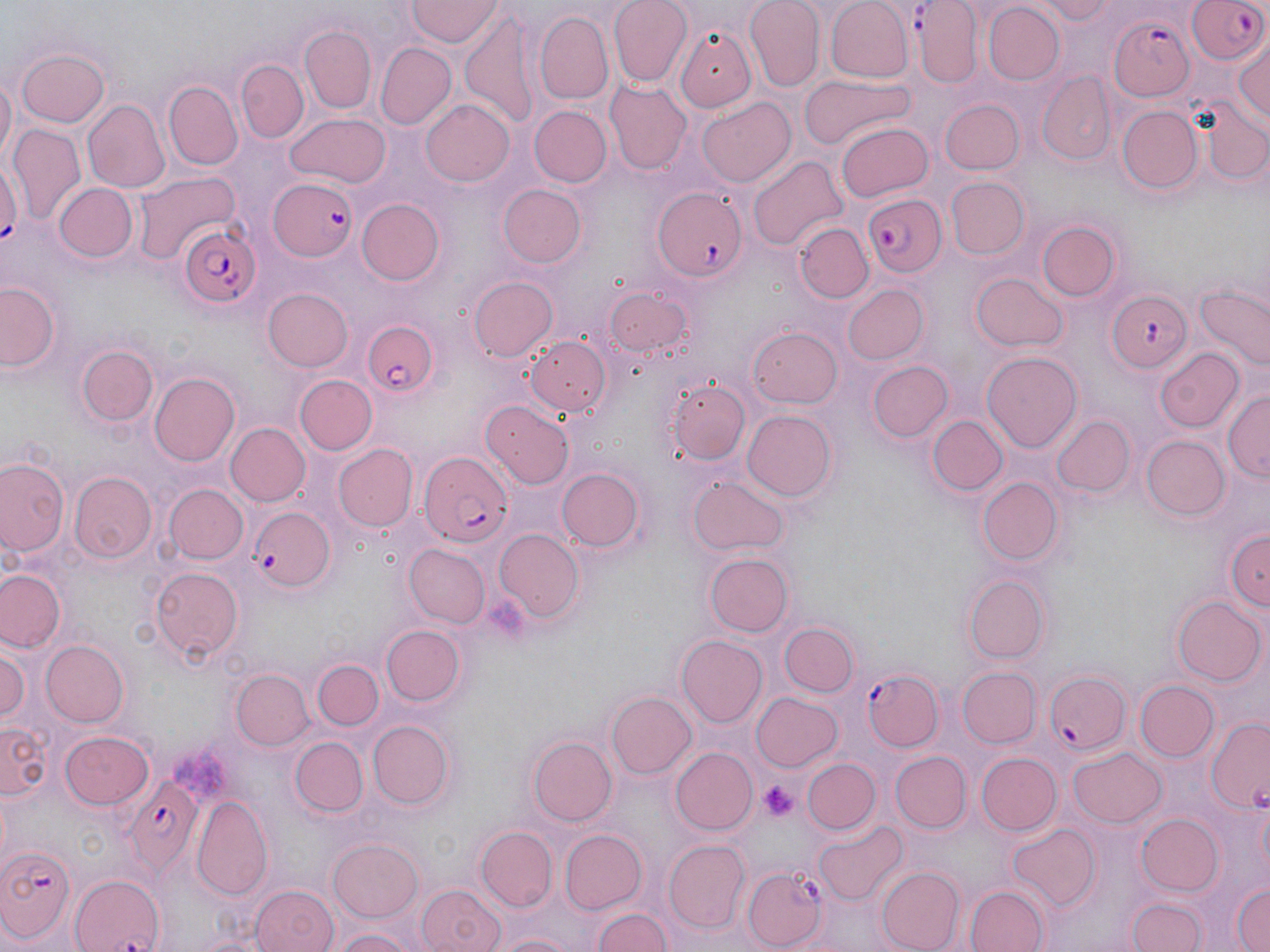
Summary:
  - Coordinate format: approximate bounding boxes as named x1/y1/x2/y2 corners in pixels
  - Platelet locations: (x1=759, y1=781, x2=801, y2=821)
  - Uninfected red blood cell locations: (x1=609, y1=0, x2=690, y2=85), (x1=746, y1=0, x2=823, y2=88), (x1=1031, y1=0, x2=1115, y2=24), (x1=824, y1=1, x2=911, y2=83), (x1=909, y1=1, x2=984, y2=85), (x1=405, y1=2, x2=502, y2=48), (x1=984, y1=3, x2=1063, y2=83), (x1=535, y1=13, x2=614, y2=101), (x1=460, y1=16, x2=542, y2=129), (x1=676, y1=24, x2=761, y2=108), (x1=296, y1=28, x2=381, y2=118), (x1=1233, y1=36, x2=1270, y2=132), (x1=376, y1=43, x2=456, y2=130), (x1=14, y1=47, x2=110, y2=128), (x1=239, y1=61, x2=307, y2=143), (x1=0, y1=71, x2=15, y2=168), (x1=799, y1=75, x2=917, y2=150), (x1=1037, y1=75, x2=1117, y2=164), (x1=164, y1=82, x2=242, y2=169), (x1=606, y1=82, x2=692, y2=175), (x1=84, y1=98, x2=169, y2=192), (x1=421, y1=98, x2=515, y2=187), (x1=699, y1=99, x2=795, y2=185), (x1=939, y1=99, x2=1024, y2=173), (x1=1195, y1=100, x2=1268, y2=190), (x1=532, y1=105, x2=610, y2=187), (x1=1119, y1=106, x2=1202, y2=193), (x1=287, y1=112, x2=390, y2=187), (x1=838, y1=122, x2=932, y2=201), (x1=8, y1=126, x2=82, y2=221), (x1=0, y1=150, x2=22, y2=254), (x1=747, y1=154, x2=848, y2=252), (x1=134, y1=173, x2=239, y2=264), (x1=946, y1=178, x2=1029, y2=258), (x1=52, y1=183, x2=139, y2=265), (x1=499, y1=184, x2=589, y2=268), (x1=358, y1=199, x2=446, y2=285), (x1=1036, y1=221, x2=1120, y2=301), (x1=795, y1=222, x2=873, y2=305), (x1=971, y1=271, x2=1068, y2=350), (x1=469, y1=277, x2=557, y2=361), (x1=2, y1=280, x2=62, y2=374), (x1=842, y1=285, x2=929, y2=364), (x1=1195, y1=287, x2=1270, y2=373), (x1=263, y1=288, x2=354, y2=372), (x1=605, y1=288, x2=696, y2=359), (x1=747, y1=324, x2=842, y2=408), (x1=525, y1=334, x2=611, y2=417), (x1=77, y1=345, x2=160, y2=428), (x1=1155, y1=347, x2=1245, y2=432), (x1=983, y1=351, x2=1083, y2=452), (x1=868, y1=360, x2=953, y2=443), (x1=663, y1=370, x2=751, y2=468), (x1=149, y1=371, x2=242, y2=466), (x1=298, y1=374, x2=377, y2=454), (x1=1224, y1=389, x2=1269, y2=484), (x1=481, y1=401, x2=576, y2=489), (x1=741, y1=410, x2=837, y2=503), (x1=928, y1=416, x2=1006, y2=495), (x1=1050, y1=416, x2=1133, y2=498), (x1=225, y1=422, x2=311, y2=506), (x1=1140, y1=436, x2=1227, y2=520), (x1=331, y1=444, x2=418, y2=533), (x1=0, y1=455, x2=70, y2=559), (x1=557, y1=468, x2=641, y2=551), (x1=72, y1=472, x2=156, y2=563), (x1=688, y1=477, x2=790, y2=555), (x1=976, y1=477, x2=1064, y2=565), (x1=165, y1=484, x2=247, y2=563), (x1=1223, y1=525, x2=1269, y2=616), (x1=493, y1=530, x2=584, y2=623), (x1=406, y1=545, x2=491, y2=628), (x1=708, y1=554, x2=791, y2=636), (x1=150, y1=565, x2=244, y2=664), (x1=1, y1=569, x2=64, y2=654), (x1=965, y1=575, x2=1049, y2=663), (x1=1173, y1=595, x2=1264, y2=685), (x1=780, y1=620, x2=857, y2=696), (x1=380, y1=625, x2=464, y2=706), (x1=676, y1=635, x2=766, y2=725), (x1=42, y1=640, x2=129, y2=727), (x1=3, y1=642, x2=33, y2=729), (x1=312, y1=660, x2=383, y2=729), (x1=958, y1=668, x2=1039, y2=747), (x1=232, y1=670, x2=312, y2=750), (x1=1138, y1=680, x2=1217, y2=762), (x1=608, y1=690, x2=696, y2=779), (x1=752, y1=693, x2=843, y2=773), (x1=1206, y1=717, x2=1270, y2=814), (x1=364, y1=719, x2=456, y2=809), (x1=2, y1=722, x2=50, y2=801), (x1=59, y1=731, x2=153, y2=810), (x1=290, y1=736, x2=366, y2=815), (x1=531, y1=736, x2=618, y2=826), (x1=1069, y1=746, x2=1166, y2=827), (x1=670, y1=748, x2=757, y2=834), (x1=889, y1=752, x2=970, y2=833), (x1=977, y1=752, x2=1061, y2=835), (x1=804, y1=757, x2=880, y2=833), (x1=192, y1=800, x2=272, y2=900), (x1=1135, y1=814, x2=1225, y2=895), (x1=813, y1=822, x2=906, y2=905), (x1=1007, y1=824, x2=1100, y2=912), (x1=474, y1=827, x2=557, y2=913), (x1=561, y1=830, x2=646, y2=913), (x1=328, y1=840, x2=424, y2=921), (x1=662, y1=841, x2=749, y2=932), (x1=878, y1=867, x2=966, y2=952), (x1=70, y1=871, x2=165, y2=952), (x1=1229, y1=879, x2=1270, y2=952), (x1=250, y1=885, x2=338, y2=952), (x1=416, y1=885, x2=505, y2=952), (x1=966, y1=885, x2=1049, y2=952), (x1=1126, y1=896, x2=1204, y2=952), (x1=591, y1=906, x2=670, y2=952), (x1=326, y1=926, x2=421, y2=952), (x1=488, y1=930, x2=581, y2=952)
  - Plasmodium falciparum-infected red blood cell locations: (x1=1186, y1=0, x2=1270, y2=66), (x1=1104, y1=12, x2=1195, y2=102), (x1=269, y1=176, x2=360, y2=260), (x1=652, y1=188, x2=747, y2=281), (x1=863, y1=192, x2=945, y2=275), (x1=178, y1=224, x2=261, y2=309), (x1=1107, y1=292, x2=1194, y2=374), (x1=360, y1=312, x2=442, y2=401), (x1=421, y1=454, x2=513, y2=547), (x1=244, y1=502, x2=336, y2=599), (x1=1043, y1=666, x2=1133, y2=755), (x1=861, y1=669, x2=944, y2=752), (x1=120, y1=775, x2=200, y2=873), (x1=0, y1=843, x2=77, y2=944), (x1=743, y1=866, x2=828, y2=950)
  - Slide-level diagnosis: Plasmodium falciparum
  - Stain: May-Grünwald-Giemsa
  - Magnification: 1000x
  - Modality: light microscopy
  - Field of view: single
  - Preparation: thin blood film
  - Image size: 1270×952 pixels